Report the malaria status of this cell.
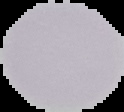
Uninfected.

Summary:
  - Image size: 124×112 pixels
  - Image type: segmented cell region on a black background
  - Preparation: thin blood film